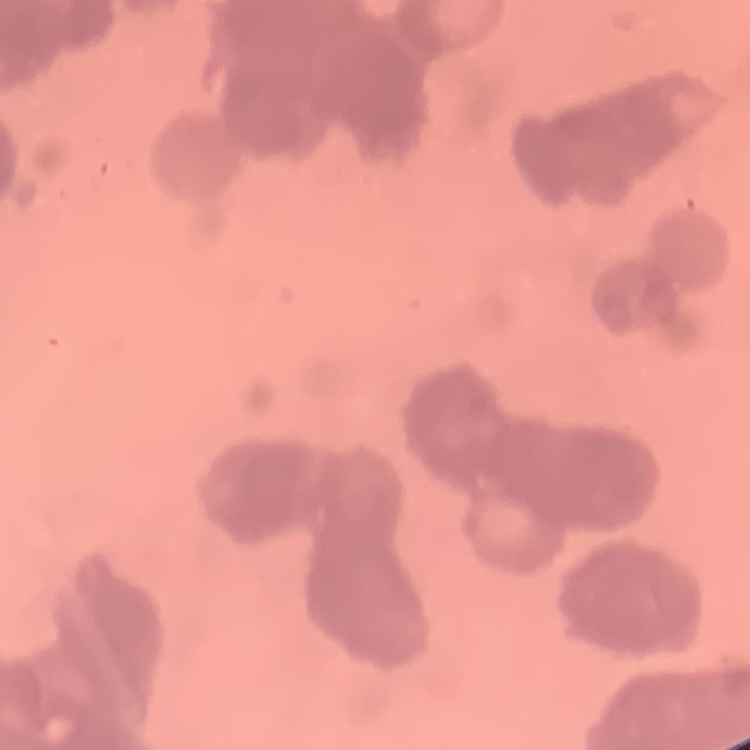

The erythrocytes show rouleaux formation. Stained with either Field's or Giemsa. Thin peripheral smear. One tile cut from a larger photomicrograph.